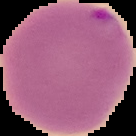
Summary:
  - Image size: 136×136 pixels
  - Preparation: thin blood smear
  - Result: malaria parasites identified
  - Image type: segmented cell region with the area outside set to black